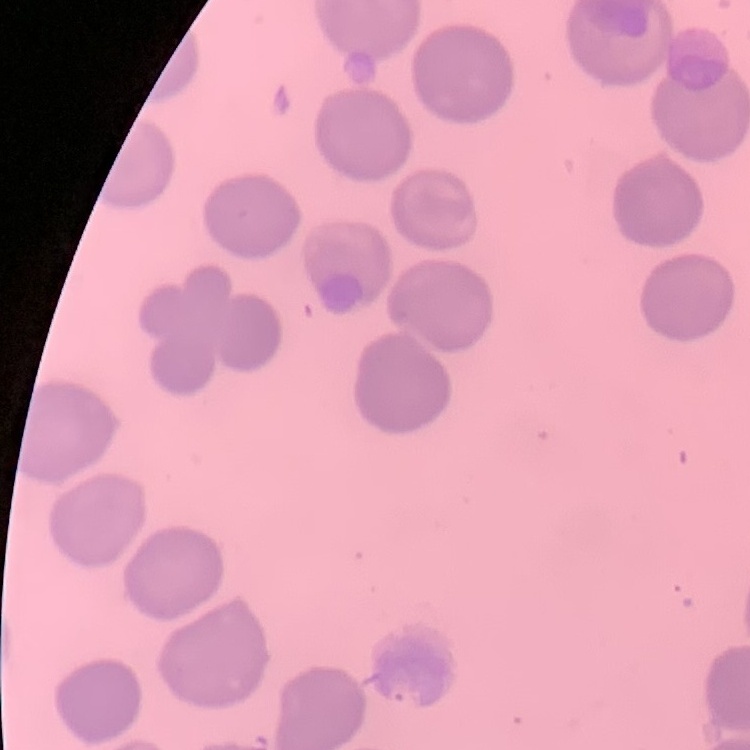
Summary:
  - Red blood cell morphology: no rouleaux formation
  - Preparation: thin blood smear
  - Stain: Field's or Giemsa
  - Image type: one tile cut from a larger photomicrograph